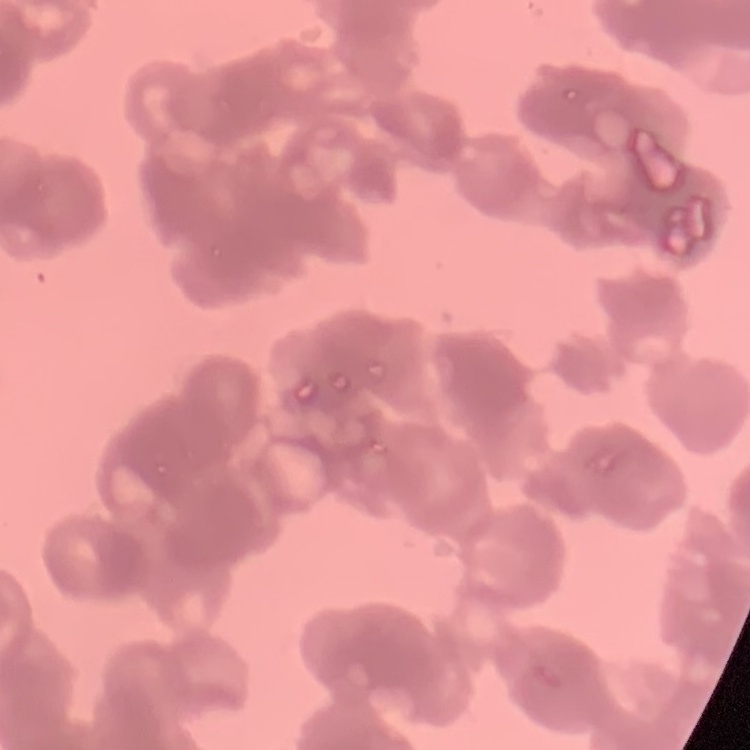 The red blood cells show rouleaux formation. Stained with either Field's or Giemsa. Thin peripheral smear. One tile cut from a larger photomicrograph.